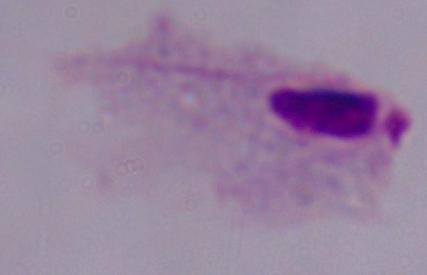
modality = micrograph
magnification = 1000x
identification = trichomonad